Locate every Plasmodium parasite.
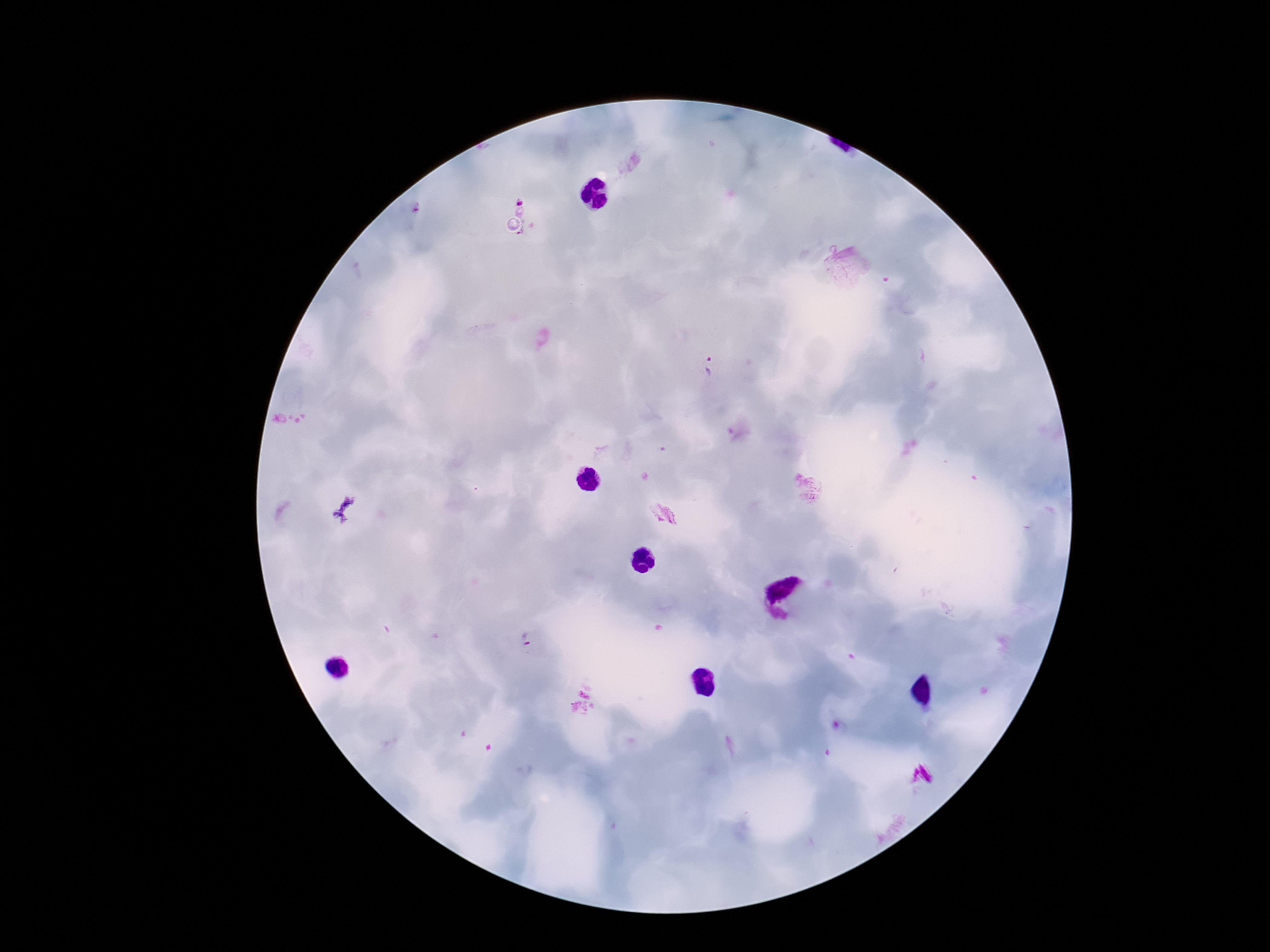

Approximate object centers, in pixels from the top-left corner.
Plasmodium parasites: (x=519, y=198), (x=527, y=229), (x=706, y=370), (x=663, y=514), (x=528, y=641).

Giemsa-stained preparation. Single field of view. Thick blood smear. 100x magnification. Photographed through the microscope eyepiece with a smartphone camera. Image is 1270×952 pixels. Patient malaria status: positive.